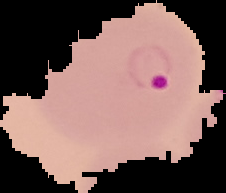 From a thin blood smear. Image is 226×193 pixels. Malaria status: parasitized. Cell region segmented out of the field of view; the surrounding area is masked to black.